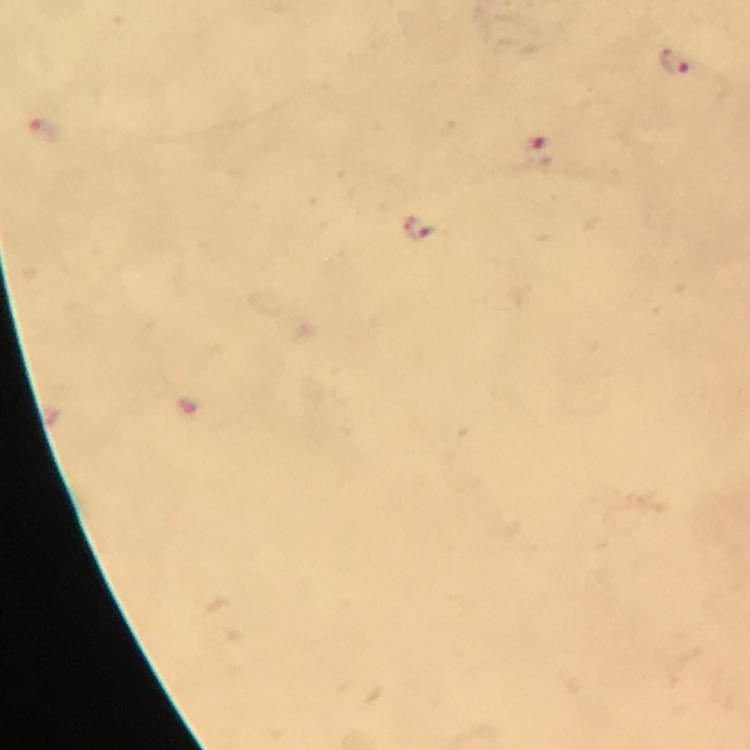
image size = 750×750 pixels
malaria parasite locations = approximate centers as {x, y} in pixels: {675, 63}, {534, 152}, {420, 228}
preparation = thick blood film
capture = smartphone photograph through a microscope
immersion oil = used
cropped from = one field of view
context = from a malaria diagnostic workup
stain = Giemsa
magnification = 100x